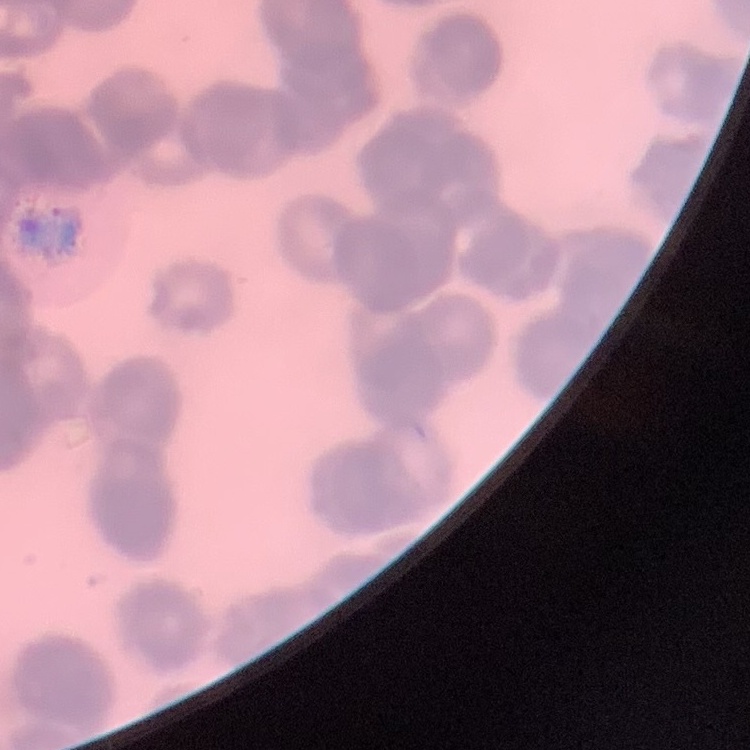

Summary:
  - Erythrocyte morphology: rouleaux formation
  - Preparation: thin blood film
  - Stain: Field's or Giemsa
  - Image type: one tile cut from a larger photomicrograph